State the blood parasite species.
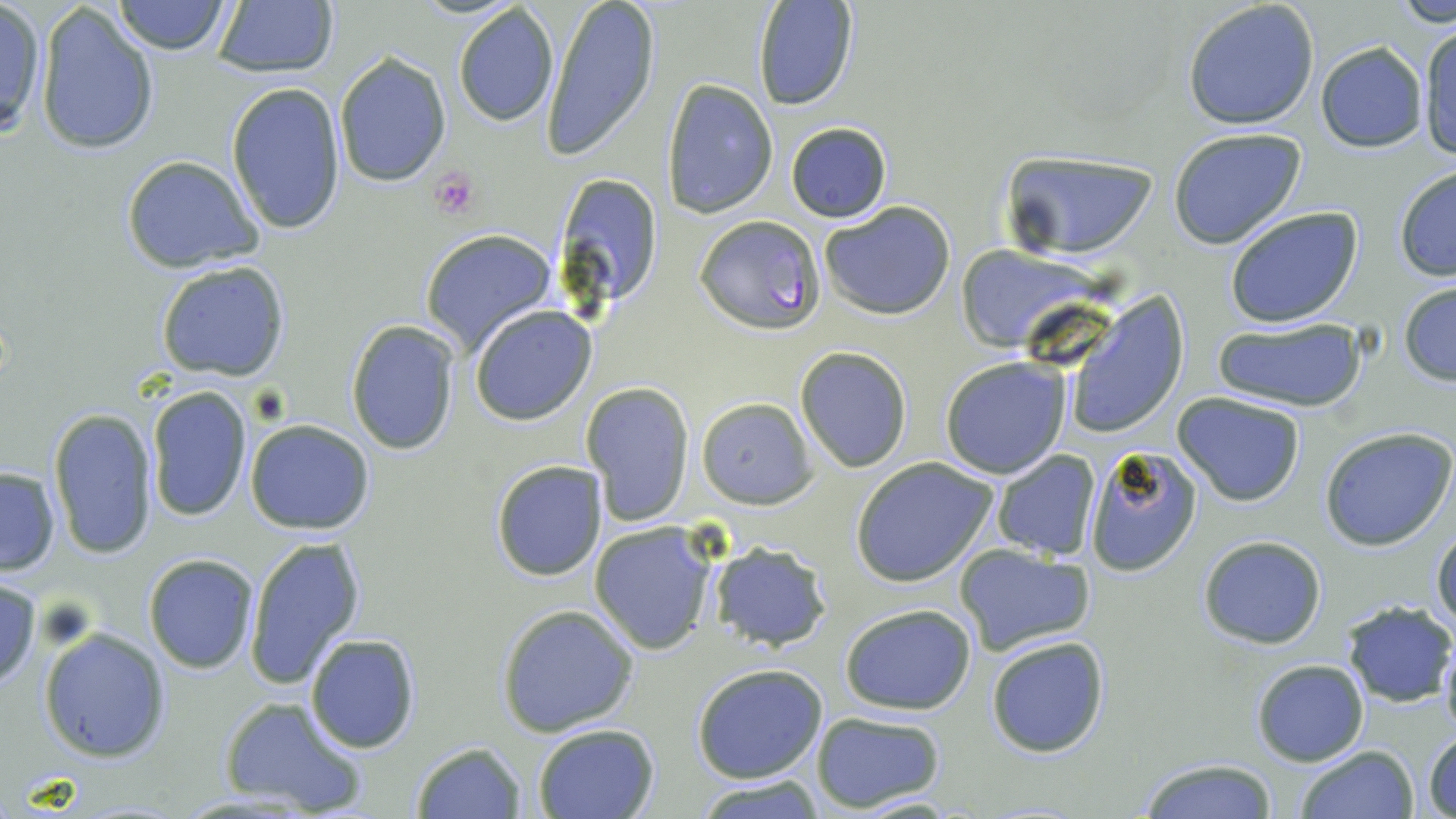

Plasmodium falciparum.

Summary:
  - Coordinate format: approximate bounding boxes as (x1, y1, x2, y2) in pixels
  - Uninfected red blood cell locations: (113, 0, 232, 55), (542, 0, 661, 162), (1392, 0, 1456, 25), (752, 1, 859, 112), (1182, 1, 1320, 130), (0, 3, 45, 140), (210, 3, 340, 80), (38, 4, 160, 156), (452, 4, 559, 126), (1418, 22, 1456, 161), (1315, 42, 1428, 151), (333, 50, 452, 189), (661, 79, 778, 218), (224, 81, 347, 235), (785, 121, 891, 223), (1167, 125, 1308, 250), (999, 149, 1159, 260), (121, 156, 262, 274), (1393, 164, 1456, 281), (550, 169, 663, 310), (818, 200, 957, 321), (1224, 206, 1364, 328), (419, 229, 558, 356), (956, 247, 1096, 350), (156, 261, 290, 382), (1398, 283, 1456, 385), (1062, 294, 1191, 441), (469, 305, 596, 426), (1213, 317, 1368, 414), (345, 319, 462, 455), (796, 347, 912, 472), (939, 358, 1071, 479), (580, 381, 696, 525), (146, 385, 252, 521), (1172, 391, 1308, 507), (148, 396, 373, 523), (695, 397, 817, 509), (47, 406, 158, 560), (245, 419, 374, 534), (1320, 427, 1456, 550), (1082, 443, 1202, 576), (991, 451, 1103, 561), (851, 457, 998, 587), (489, 459, 609, 581), (0, 466, 60, 575), (589, 522, 719, 655), (1431, 527, 1456, 636), (242, 533, 367, 689), (1197, 535, 1326, 649), (708, 540, 834, 651), (954, 545, 1099, 659), (143, 554, 260, 674), (0, 575, 42, 694), (1339, 601, 1453, 707), (495, 603, 638, 737), (838, 603, 978, 715), (38, 628, 171, 762), (303, 633, 421, 755), (985, 633, 1111, 757), (1438, 639, 1456, 742), (1250, 659, 1369, 767), (691, 663, 830, 784), (217, 696, 368, 818), (810, 711, 948, 812), (531, 724, 660, 818), (1423, 731, 1456, 817), (410, 741, 526, 818), (1295, 745, 1418, 819), (1135, 757, 1282, 818), (694, 776, 825, 817)
  - Platelet locations: (430, 167, 482, 220)
  - Plasmodium falciparum-infected red blood cell locations: (697, 216, 826, 333)
  - Magnification: 1000x
  - Stain: May-Grünwald-Giemsa
  - Field of view: single
  - Modality: optical microscopy
  - Preparation: thin blood smear
  - Image size: 1456×819 pixels